Name the parasite shown.
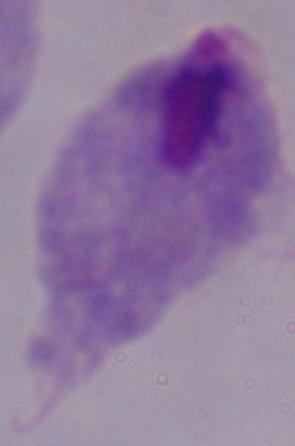

A trichomonad.

modality = photomicrograph
magnification = 1000x